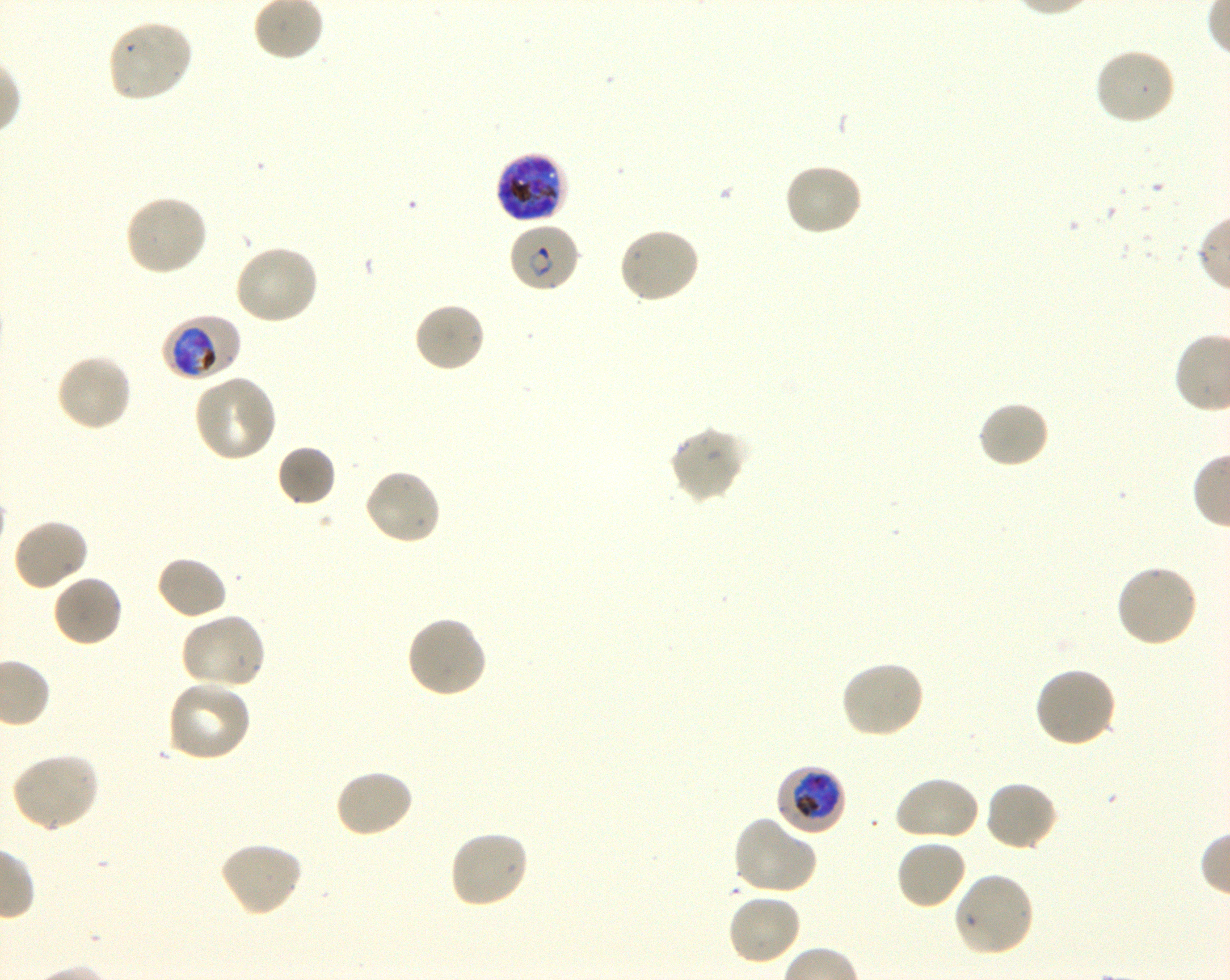
Approximate bounding rectangles given as corner coordinates in pixels from the top-left. Not every red blood cell is marked. A life-cycle stage — or a range of stages, where the recorded stages span more than one — follows each staged infected red blood cell. Locations of infected red blood cells: (x1=494, y1=152, x2=568, y2=225) late trophozoite to late schizont; (x1=507, y1=221, x2=581, y2=294) ring; (x1=162, y1=314, x2=241, y2=381) trophozoite; (x1=775, y1=764, x2=846, y2=835) early trophozoite to early schizont. Locations of uninfected red blood cells: (x1=106, y1=19, x2=194, y2=104), (x1=1093, y1=46, x2=1177, y2=126), (x1=782, y1=162, x2=864, y2=237), (x1=123, y1=194, x2=209, y2=277), (x1=618, y1=226, x2=701, y2=305), (x1=233, y1=243, x2=320, y2=326), (x1=412, y1=301, x2=487, y2=374), (x1=54, y1=352, x2=132, y2=433), (x1=193, y1=374, x2=278, y2=463), (x1=977, y1=400, x2=1051, y2=471), (x1=669, y1=425, x2=749, y2=504), (x1=276, y1=444, x2=337, y2=507), (x1=363, y1=467, x2=443, y2=546), (x1=12, y1=517, x2=89, y2=592), (x1=155, y1=555, x2=229, y2=621), (x1=1114, y1=563, x2=1200, y2=649), (x1=51, y1=573, x2=123, y2=648), (x1=179, y1=612, x2=267, y2=690), (x1=404, y1=615, x2=488, y2=700), (x1=838, y1=660, x2=926, y2=739), (x1=1032, y1=666, x2=1117, y2=749), (x1=166, y1=678, x2=253, y2=763), (x1=9, y1=752, x2=101, y2=832), (x1=333, y1=768, x2=416, y2=840), (x1=893, y1=774, x2=981, y2=843), (x1=983, y1=779, x2=1059, y2=853), (x1=733, y1=815, x2=818, y2=896), (x1=447, y1=828, x2=531, y2=909), (x1=895, y1=837, x2=968, y2=910), (x1=218, y1=841, x2=303, y2=918), (x1=952, y1=871, x2=1036, y2=958), (x1=726, y1=892, x2=802, y2=966). Life-cycle stages observed: ring, trophozoite. Blood group of the donor: O+. Thin blood film. Oil immersion, 100x objective (numerical aperture 1.30). One field from this slide. Plasmodium falciparum strain 3D7 in shaking in-vitro culture. Image is 1230×980 pixels. Giemsa-stained preparation.